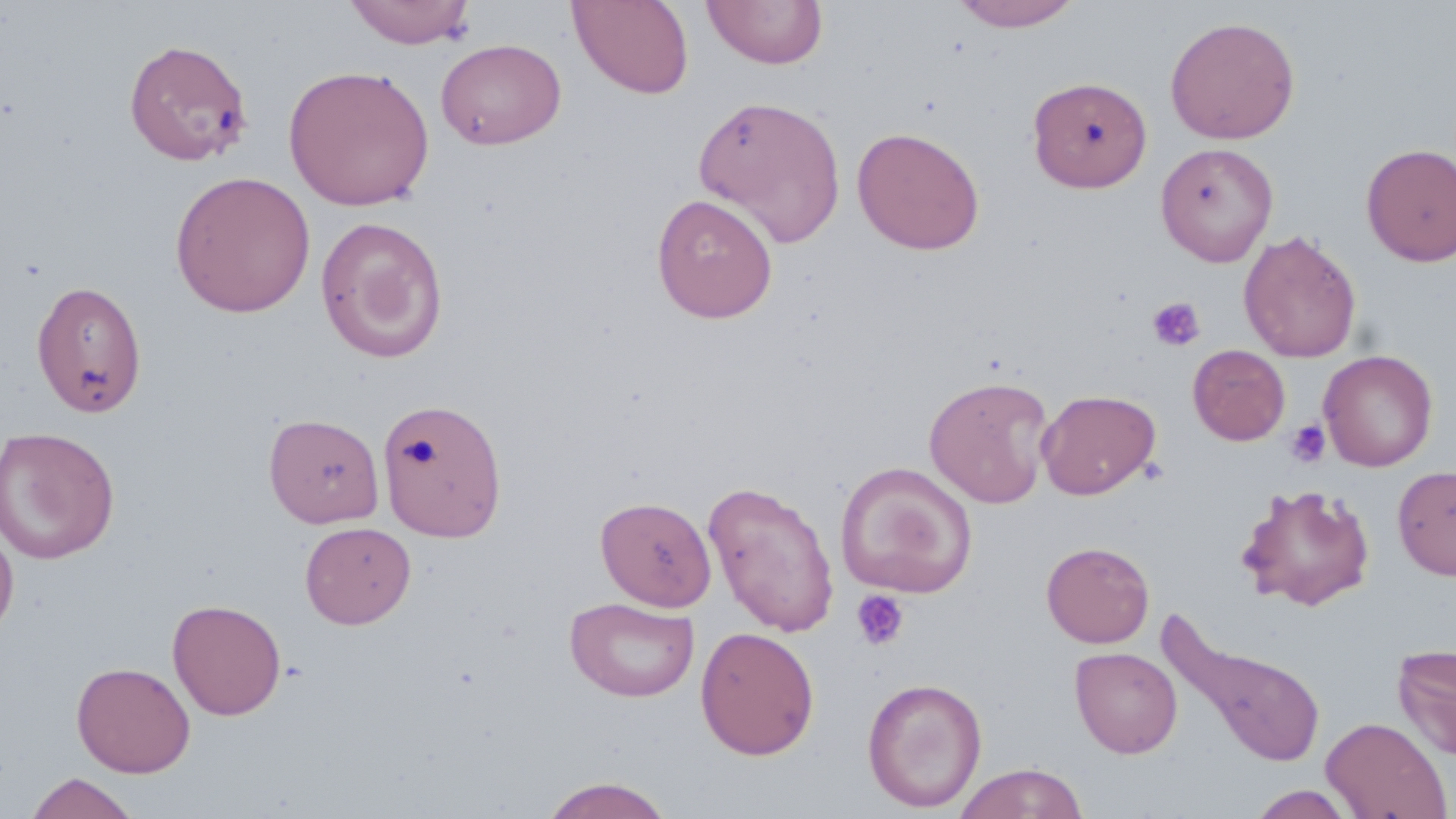 Approximate bounding boxes as (x1,y1)-(x2,y2) corner pairs in pixels. Uninfected red blood cell locations: (344,0)-(477,48), (567,0)-(695,99), (702,1)-(828,69), (951,1)-(1082,31), (1165,15)-(1300,145), (123,38)-(253,166), (435,38)-(566,149), (283,64)-(435,211), (1027,76)-(1152,192), (693,94)-(846,246), (852,126)-(985,255), (1154,141)-(1279,266), (1360,142)-(1456,266), (170,171)-(316,318), (651,193)-(778,323), (315,216)-(449,363), (1239,230)-(1362,363), (31,280)-(147,418), (1188,344)-(1290,445), (1318,349)-(1438,471), (924,375)-(1054,508), (1037,388)-(1161,499), (377,398)-(508,542), (264,412)-(384,527), (0,426)-(120,564), (835,460)-(978,599), (1393,465)-(1456,581), (703,479)-(841,637), (1235,481)-(1376,611), (595,495)-(716,611), (0,520)-(19,647), (300,521)-(416,629), (1041,541)-(1155,648), (565,596)-(700,703), (167,598)-(287,720), (695,626)-(820,760), (1166,626)-(1326,770), (1393,644)-(1456,760), (1070,647)-(1182,758), (71,661)-(195,777), (862,677)-(987,812), (1321,716)-(1451,818), (954,762)-(1089,819), (25,772)-(141,818), (537,776)-(677,818), (1246,784)-(1360,819). Platelet locations: (1147,297)-(1205,352), (1285,420)-(1331,468), (851,590)-(910,650). Slide-level diagnosis: no evidence of blood parasites. Thin blood film. Optical microscopy. Image is 1456×819 pixels. Captured at 1000x magnification. May-Grünwald-Giemsa stain. One field of a larger specimen.